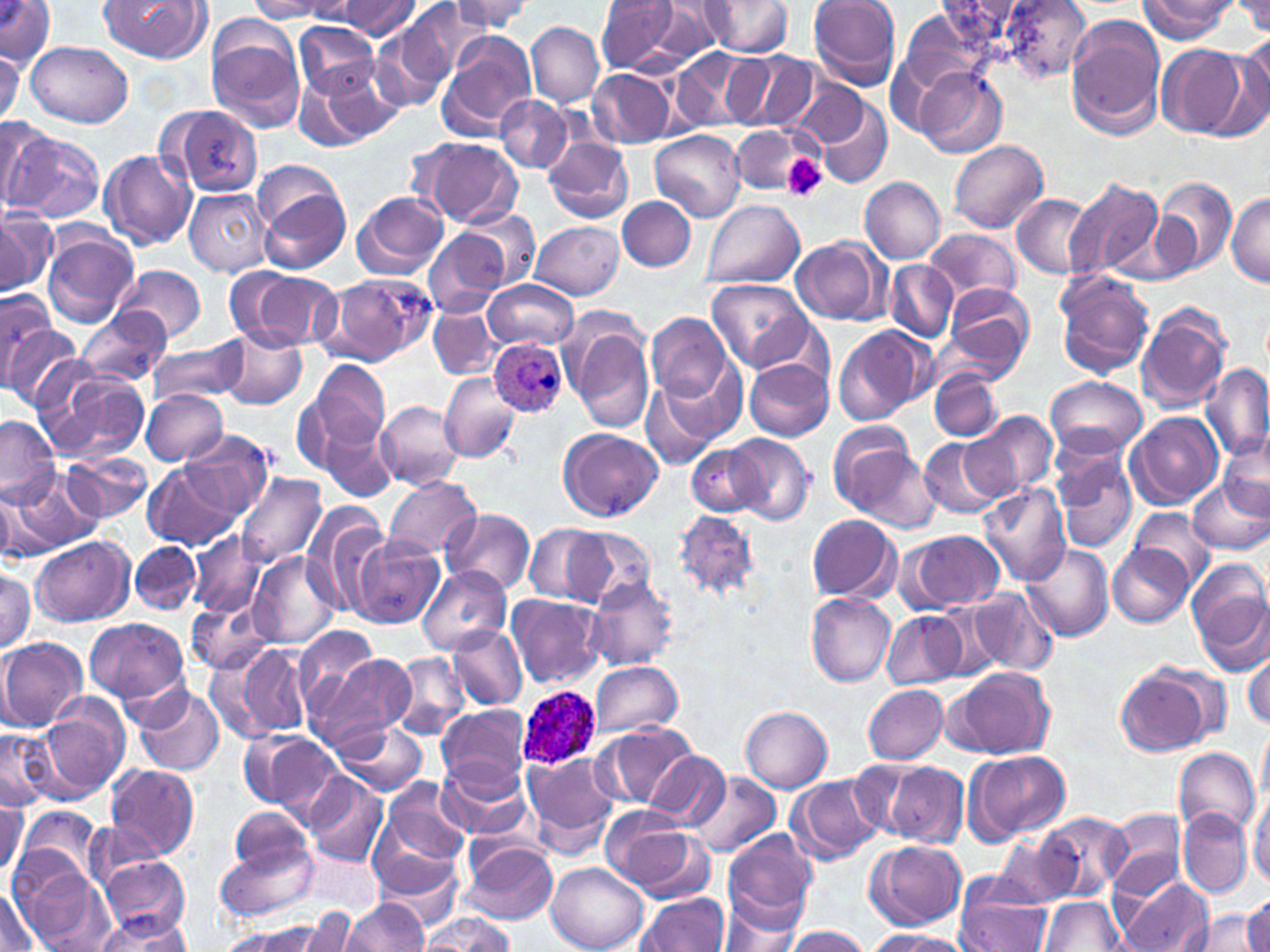
Summary:
  - Coordinate format: approximate bounding boxes as [x1, y1, x2, y2] in pixels
  - Platelet locations: [780, 153, 828, 201]
  - Uninfected red blood cell locations: [0, 0, 56, 71], [98, 0, 210, 62], [335, 0, 422, 38], [449, 0, 532, 34], [595, 0, 680, 74], [808, 0, 902, 91], [1002, 0, 1090, 81], [1234, 0, 1269, 36], [249, 1, 334, 21], [648, 1, 728, 60], [702, 1, 793, 57], [1137, 1, 1240, 41], [400, 2, 491, 82], [423, 2, 521, 57], [1067, 17, 1167, 139], [294, 21, 382, 99], [205, 22, 308, 133], [371, 22, 455, 111], [527, 22, 603, 106], [438, 33, 536, 139], [1221, 37, 1270, 137], [886, 40, 980, 139], [26, 41, 133, 128], [1155, 45, 1250, 139], [0, 48, 22, 128], [672, 48, 757, 131], [722, 52, 815, 133], [296, 65, 395, 147], [913, 68, 1006, 158], [590, 69, 673, 148], [786, 79, 872, 149], [495, 93, 575, 174], [810, 98, 892, 190], [167, 105, 266, 197], [0, 118, 49, 210], [729, 125, 807, 197], [3, 129, 103, 226], [650, 130, 747, 221], [416, 136, 523, 226], [543, 136, 633, 224], [949, 141, 1048, 234], [100, 150, 196, 250], [256, 177, 353, 275], [859, 177, 946, 263], [1064, 178, 1166, 279], [1156, 179, 1236, 278], [185, 189, 273, 275], [352, 192, 448, 279], [1225, 193, 1270, 288], [1012, 194, 1096, 277], [618, 196, 696, 271], [703, 199, 804, 289], [1, 206, 58, 295], [459, 209, 538, 288], [531, 222, 625, 299], [423, 229, 511, 317], [923, 229, 1022, 303], [42, 230, 138, 326], [790, 237, 889, 325], [886, 262, 958, 341], [114, 264, 206, 344], [237, 268, 341, 351], [1055, 272, 1155, 380], [319, 275, 428, 367], [706, 277, 815, 374], [484, 280, 578, 350], [939, 283, 1035, 377], [0, 289, 59, 383], [1136, 303, 1235, 416], [428, 304, 498, 379], [77, 309, 172, 386], [561, 312, 656, 433], [647, 314, 732, 402], [217, 323, 307, 411], [834, 324, 929, 426], [4, 325, 84, 411], [150, 340, 248, 407], [658, 356, 750, 447], [304, 359, 393, 462], [745, 360, 833, 441], [34, 363, 148, 463], [1201, 363, 1270, 467], [929, 369, 1003, 441], [440, 372, 523, 463], [1045, 376, 1147, 460], [640, 378, 724, 470], [140, 387, 229, 465], [376, 401, 464, 493], [962, 408, 1056, 501], [1128, 411, 1223, 508], [0, 416, 61, 503], [829, 423, 916, 510], [322, 424, 399, 501], [559, 427, 663, 520], [181, 428, 277, 519], [727, 434, 813, 527], [1220, 434, 1270, 517], [919, 435, 1005, 519], [837, 443, 942, 534], [687, 445, 766, 517], [62, 452, 152, 524], [1056, 453, 1136, 554], [144, 462, 237, 548], [1, 469, 97, 559], [234, 472, 328, 570], [384, 475, 480, 561], [1187, 476, 1269, 556], [978, 483, 1073, 585], [302, 501, 391, 616], [440, 507, 536, 596], [1128, 507, 1216, 591], [673, 510, 760, 601], [807, 514, 899, 601], [526, 523, 607, 605], [563, 527, 655, 610], [189, 531, 266, 619], [908, 532, 1004, 613], [349, 533, 443, 629], [31, 538, 132, 626], [129, 540, 200, 614], [1107, 542, 1192, 627], [1021, 543, 1114, 642], [248, 552, 342, 652], [1187, 564, 1270, 674], [416, 565, 512, 656], [0, 567, 36, 652], [585, 578, 678, 671], [186, 589, 278, 673], [969, 589, 1057, 676], [807, 593, 896, 686], [506, 594, 606, 688], [936, 604, 1009, 679], [883, 611, 967, 689], [84, 616, 189, 705], [447, 626, 527, 711], [292, 627, 386, 718], [0, 637, 86, 732], [233, 644, 311, 737], [1244, 651, 1269, 729], [304, 653, 414, 754], [388, 654, 470, 741], [587, 660, 683, 737], [1114, 663, 1219, 758], [947, 667, 1054, 760], [133, 684, 224, 776], [863, 685, 948, 763], [437, 705, 533, 787], [741, 706, 832, 793], [32, 707, 127, 803], [338, 721, 428, 796], [593, 723, 699, 810], [0, 727, 53, 812], [240, 727, 343, 817], [1258, 728, 1270, 808], [1172, 748, 1259, 838], [965, 750, 1071, 843], [645, 752, 733, 831], [524, 753, 619, 852], [436, 757, 533, 841], [861, 758, 969, 848], [106, 764, 198, 862], [687, 772, 780, 858], [305, 774, 387, 867], [790, 774, 885, 864], [378, 780, 471, 872], [1249, 786, 1270, 883], [0, 791, 27, 878], [598, 806, 705, 897], [19, 807, 102, 888], [228, 808, 316, 880], [1104, 808, 1186, 894], [1179, 809, 1250, 897], [1040, 813, 1131, 900], [723, 828, 819, 925], [995, 834, 1082, 907], [460, 838, 560, 925], [215, 839, 319, 923], [865, 839, 966, 930], [372, 849, 463, 927], [98, 857, 188, 938], [546, 862, 648, 952], [17, 868, 113, 952], [1117, 874, 1215, 952], [957, 880, 1057, 952], [0, 886, 43, 952], [637, 892, 730, 952], [1041, 895, 1123, 950], [1241, 895, 1270, 952], [343, 898, 428, 951], [719, 905, 804, 952], [94, 910, 191, 951], [294, 910, 362, 952], [1183, 910, 1260, 950], [424, 913, 514, 951], [225, 921, 335, 952], [780, 926, 869, 951], [866, 929, 968, 952]
  - Plasmodium ovale-infected red blood cell locations: [488, 338, 568, 418], [513, 685, 603, 770]
  - Slide-level diagnosis: Plasmodium ovale
  - Field of view: single
  - Modality: optical microscopy
  - Preparation: thin blood smear
  - Magnification: 1000x
  - Stain: May-Grünwald-Giemsa
  - Image size: 1270×952 pixels